Locate every Plasmodium falciparum-infected red blood cell.
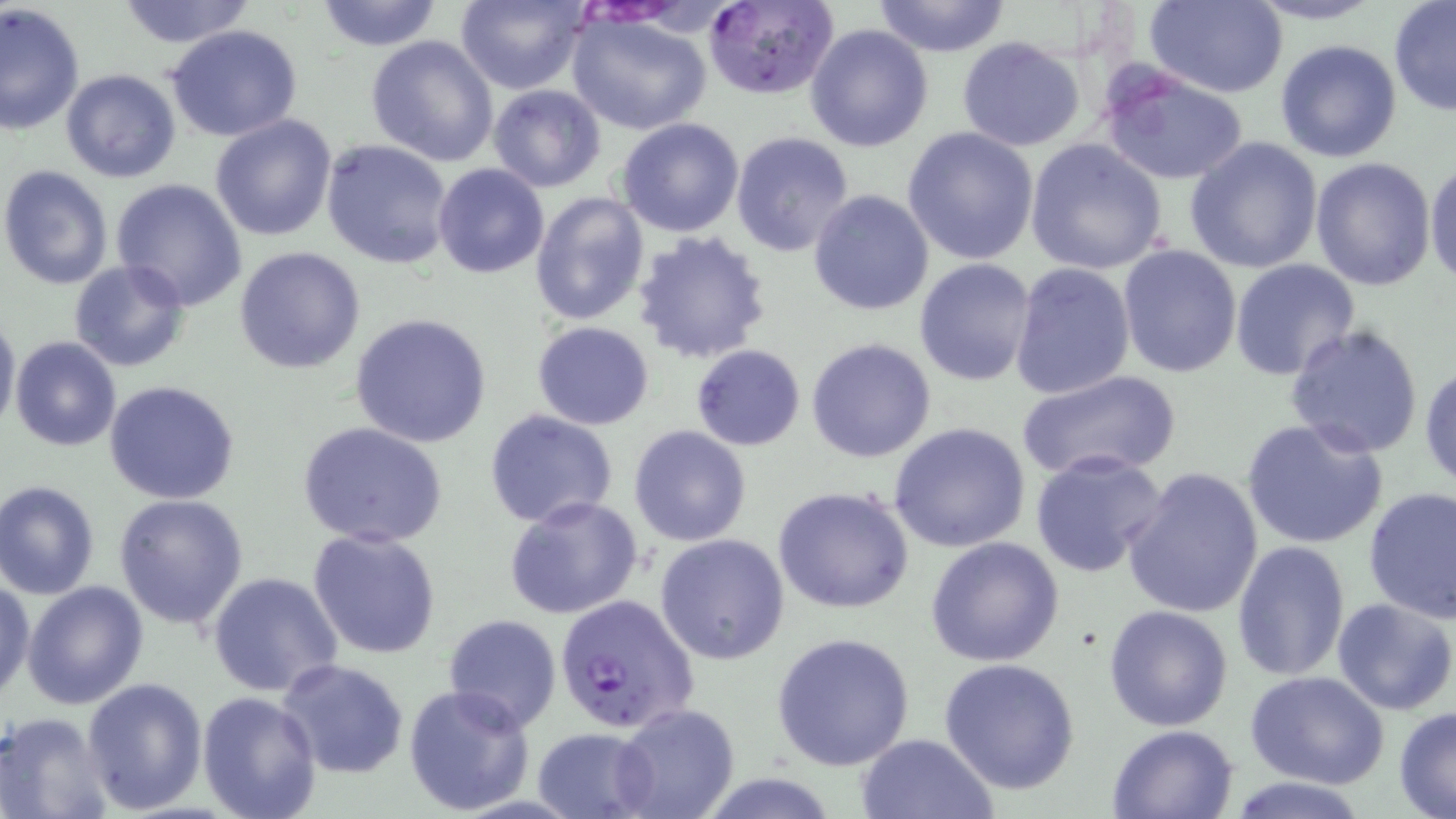

Approximate bounding boxes as (x1,y1)-(x2,y2) corner pairs in pixels.
Plasmodium falciparum-infected red blood cells: (703,1)-(840,100), (556,591)-(702,734).

Uninfected red blood cell locations: (112,0)-(257,49), (312,0)-(445,51), (455,0)-(590,94), (1146,0)-(1288,97), (1243,0)-(1386,26), (1388,1)-(1456,117), (871,2)-(1013,56), (0,3)-(85,136), (566,12)-(714,135), (166,24)-(303,142), (805,24)-(934,153), (365,35)-(500,166), (956,37)-(1085,152), (1274,40)-(1403,164), (1098,63)-(1250,186), (60,69)-(182,183), (487,84)-(606,193), (210,114)-(340,242), (616,118)-(745,238), (902,126)-(1039,266), (732,132)-(856,259), (1184,136)-(1323,273), (322,139)-(452,269), (1024,139)-(1169,275), (1309,156)-(1437,290), (1425,158)-(1456,287), (432,163)-(550,279), (0,165)-(114,290), (111,178)-(249,311), (808,189)-(934,316), (530,190)-(651,326), (631,231)-(773,364), (1116,243)-(1242,379), (234,245)-(366,374), (1230,258)-(1359,380), (68,259)-(191,373), (915,259)-(1038,386), (1009,261)-(1137,400), (0,310)-(20,437), (351,313)-(493,449), (533,320)-(655,429), (1285,322)-(1426,458), (11,337)-(123,453), (806,337)-(936,463), (690,343)-(807,451), (1420,362)-(1456,492), (1014,369)-(1184,482), (104,380)-(240,504), (484,410)-(618,529), (1241,416)-(1390,551), (297,420)-(449,550), (888,421)-(1031,553), (628,425)-(753,547), (1029,448)-(1169,579), (1122,467)-(1263,619), (1,479)-(101,599), (772,485)-(916,614), (1363,485)-(1456,624), (114,493)-(249,630), (504,494)-(645,622), (305,528)-(444,660), (654,534)-(790,664), (924,535)-(1065,667), (1232,540)-(1351,682), (207,570)-(344,697), (0,577)-(34,703), (22,579)-(149,709), (1331,597)-(1456,716), (1102,604)-(1233,733), (442,614)-(561,730), (770,632)-(917,771), (278,657)-(410,780), (940,657)-(1081,794), (1246,672)-(1390,789), (81,676)-(208,814), (403,683)-(535,817), (196,690)-(321,819), (612,704)-(742,819), (1393,706)-(1456,818), (0,711)-(115,819), (1106,723)-(1242,818), (532,726)-(657,819), (855,733)-(998,818), (1226,776)-(1370,818). Slide-level diagnosis: Plasmodium falciparum. One field of a larger specimen. May-Grünwald-Giemsa stain. Image is 1456×819 pixels. Thin blood smear. Optical microscopy. Captured at 1000x magnification.